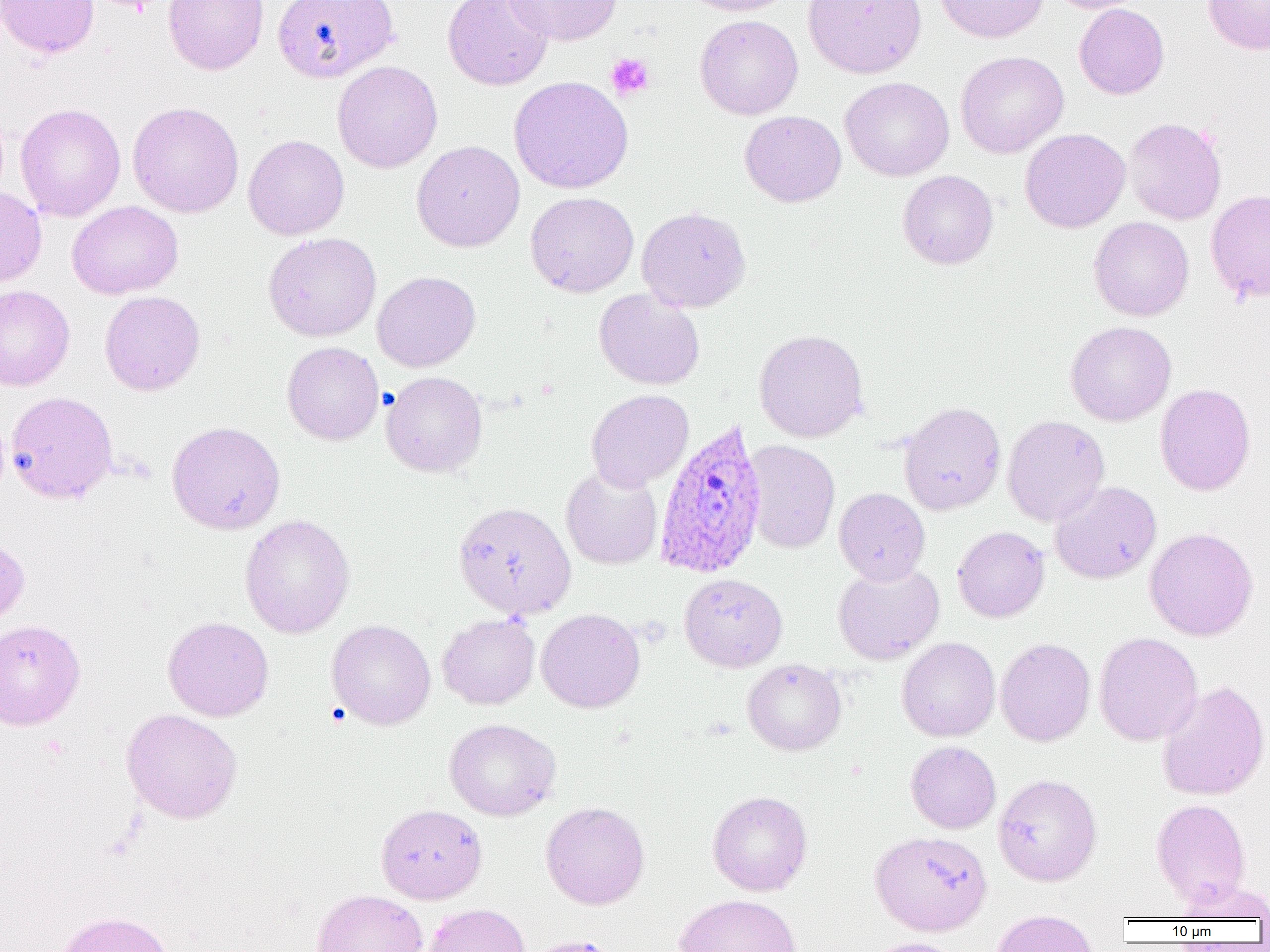

slide-level diagnosis = Plasmodium ovale
platelet locations = approximate bounding boxes as (x1,y1)-(x2,y2) corner pairs in pixels: (97,0)-(162,15), (605,53)-(655,101)
image size = 1270×952 pixels
modality = light microscopy
Plasmodium ovale-infected red blood cell locations = approximate bounding boxes as (x1,y1)-(x2,y2) corner pairs in pixels: (653,417)-(768,578)
uninfected red blood cell locations = approximate bounding boxes as (x1,y1)-(x2,y2) corner pairs in pixels: (0,0)-(99,58), (163,0)-(269,75), (272,0)-(399,83), (442,0)-(554,91), (503,0)-(622,46), (676,0)-(798,16), (803,0)-(926,79), (934,0)-(1048,43), (1047,0)-(1149,14), (1203,0)-(1270,55), (1073,3)-(1169,99), (695,15)-(803,119), (955,51)-(1069,159), (332,61)-(443,173), (509,76)-(633,194), (840,77)-(954,181), (127,101)-(244,218), (15,103)-(125,222), (740,110)-(846,207), (1123,117)-(1227,225), (1020,128)-(1131,233), (243,134)-(349,240), (411,140)-(525,252), (898,170)-(998,269), (0,187)-(47,286), (1206,190)-(1270,303), (525,192)-(639,297), (67,201)-(184,299), (637,206)-(751,313), (1089,216)-(1194,321), (263,232)-(381,341), (372,270)-(481,372), (0,285)-(75,391), (593,289)-(705,390), (99,290)-(205,396), (1065,321)-(1176,426), (754,329)-(869,442), (281,341)-(384,445), (381,371)-(488,477), (1155,383)-(1255,495), (586,389)-(694,491), (5,391)-(117,504), (898,401)-(1006,515), (1002,414)-(1109,526), (166,421)-(286,535), (742,440)-(840,553), (561,465)-(663,569), (1050,481)-(1162,584), (834,487)-(930,585), (453,501)-(576,620), (240,514)-(355,638), (952,526)-(1050,622), (1145,527)-(1258,641), (0,533)-(30,627), (832,562)-(944,664), (679,573)-(787,672), (536,608)-(645,713), (437,614)-(540,709), (163,616)-(274,721), (0,618)-(86,730), (327,619)-(436,730), (1093,632)-(1202,746), (897,637)-(1000,742), (995,638)-(1095,746), (742,658)-(846,755), (1156,680)-(1270,801), (121,708)-(242,823), (444,718)-(561,821), (906,741)-(1001,833), (993,774)-(1102,886), (707,790)-(812,896), (1151,798)-(1251,906), (540,801)-(649,909), (376,803)-(487,904), (870,831)-(993,936), (1176,878)-(1270,921), (311,889)-(428,952), (675,893)-(802,952), (424,903)-(531,952), (991,909)-(1099,952), (54,910)-(174,952), (521,935)-(622,952), (864,937)-(964,952)
preparation = thin blood smear
field of view = one of a larger specimen
magnification = 1000x